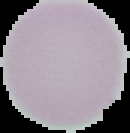 From a thin blood smear. Segmented cell region on a black background. Malaria status: uninfected. Image is 130×133 pixels.